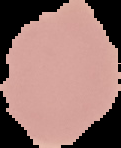
image_size: 121×148 pixels
result: no Plasmodium parasites seen
preparation: thin blood smear
image_type: cell region segmented out of the field of view; surrounding area masked to black